Assess this cell for malaria.
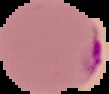

It is parasitized.

Segmented cell region on a black background. From a thin blood film. Image is 109×94 pixels.